Report the malaria status of this cell.
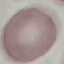

Uninfected.

{
  "preparation": "thin blood film",
  "stain": "Giemsa",
  "capture": "smartphone camera at the microscope eyepiece",
  "image_type": "cell patch, automatically extracted from a larger field of view and resized to 64 × 64 pixels"
}